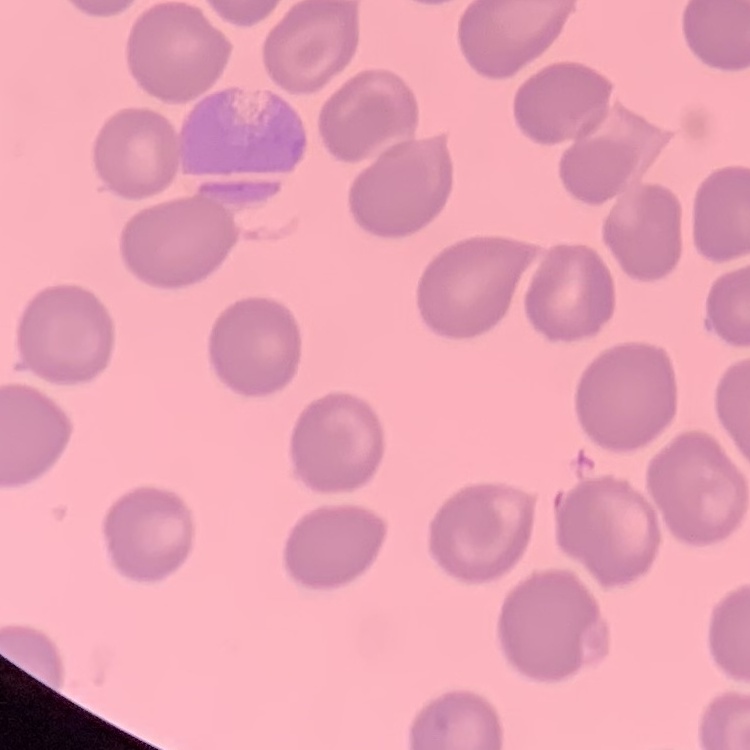

Summary:
  - Red blood cell morphology: no rouleaux formation
  - Preparation: thin blood smear
  - Image type: one tile cut from a larger photomicrograph
  - Stain: Field's or Giemsa